Outline each Plasmodium malariae-infected red blood cell.
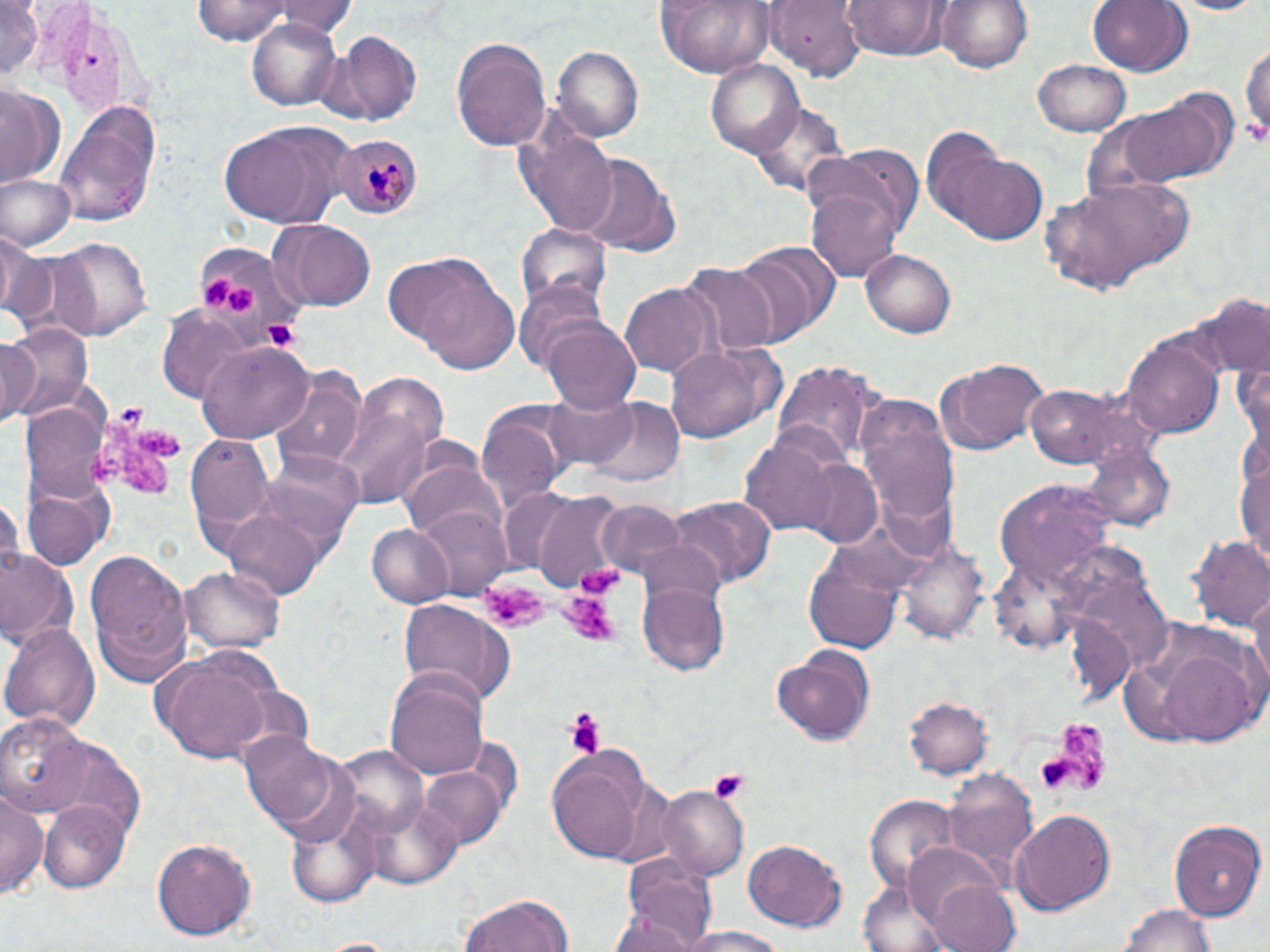
Approximate bounding boxes as (x1, y1, x2, y2) in pixels.
Plasmodium malariae-infected red blood cells: (334, 133, 423, 220).

Uninfected red blood cell locations: (195, 0, 292, 46), (275, 0, 354, 37), (840, 0, 950, 61), (936, 0, 1034, 72), (1087, 0, 1191, 77), (1167, 0, 1264, 15), (0, 1, 42, 82), (653, 1, 775, 76), (765, 1, 864, 80), (245, 19, 342, 112), (327, 31, 424, 125), (451, 34, 550, 152), (1241, 35, 1269, 150), (551, 44, 644, 144), (1035, 58, 1131, 138), (706, 60, 804, 156), (0, 86, 65, 190), (1129, 91, 1236, 185), (751, 100, 850, 200), (55, 102, 160, 227), (218, 119, 358, 227), (522, 125, 619, 235), (923, 130, 1042, 244), (804, 143, 922, 256), (571, 153, 681, 256), (3, 174, 75, 253), (1041, 176, 1192, 296), (806, 184, 905, 283), (269, 221, 376, 311), (518, 222, 609, 312), (1, 228, 48, 326), (50, 236, 153, 338), (193, 237, 299, 337), (731, 242, 835, 345), (864, 250, 955, 338), (401, 263, 523, 373), (679, 264, 778, 357), (517, 281, 612, 372), (620, 283, 721, 377), (1201, 294, 1269, 379), (158, 306, 259, 404), (544, 321, 643, 415), (3, 322, 94, 419), (0, 335, 41, 427), (1125, 336, 1225, 438), (663, 339, 785, 446), (198, 341, 314, 441), (937, 356, 1049, 455), (771, 361, 881, 467), (271, 371, 367, 471), (355, 373, 449, 462), (1025, 383, 1148, 471), (545, 392, 639, 473), (581, 397, 686, 486), (856, 399, 956, 522), (20, 401, 110, 508), (476, 404, 572, 508), (337, 406, 437, 505), (742, 432, 848, 535), (186, 436, 275, 537), (259, 452, 363, 546), (1235, 456, 1270, 560), (792, 457, 886, 548), (401, 460, 503, 546), (994, 481, 1119, 588), (25, 485, 108, 570), (498, 488, 585, 577), (530, 491, 629, 592), (667, 494, 778, 590), (0, 495, 24, 577), (594, 497, 690, 579), (411, 506, 510, 597), (219, 508, 330, 601), (366, 524, 454, 606), (1190, 534, 1270, 633), (898, 540, 987, 648), (801, 542, 901, 654), (84, 548, 195, 687), (0, 550, 77, 647), (182, 567, 282, 654), (639, 579, 730, 677), (1248, 586, 1269, 695), (397, 599, 516, 703), (1118, 616, 1269, 748), (2, 621, 99, 735), (770, 643, 877, 745), (151, 651, 280, 764), (386, 672, 489, 782), (903, 696, 992, 781), (0, 714, 97, 812), (239, 732, 347, 833), (331, 744, 428, 835), (548, 749, 647, 862), (422, 765, 507, 847), (943, 767, 1040, 881), (1, 785, 47, 900), (658, 788, 747, 876), (864, 795, 964, 896), (362, 796, 461, 890), (40, 802, 129, 893), (286, 806, 384, 908), (1011, 810, 1115, 914), (1168, 817, 1264, 923), (152, 838, 257, 942), (741, 839, 850, 934), (903, 842, 1005, 930), (622, 855, 720, 949), (928, 878, 1022, 952), (457, 893, 574, 952), (1118, 900, 1218, 952), (608, 903, 708, 951), (672, 927, 799, 952). Platelet locations: (1243, 116, 1266, 147), (200, 273, 235, 307), (226, 286, 257, 315), (259, 318, 304, 353), (96, 410, 179, 497), (484, 576, 548, 632), (560, 581, 623, 648), (562, 707, 608, 755), (1038, 719, 1109, 798), (706, 769, 750, 799). Slide-level diagnosis: Plasmodium malariae. Optical microscopy. Single field of view. Thin blood film. Image is 1270×952 pixels. Captured at 1000x magnification. May-Grünwald-Giemsa-stained preparation.